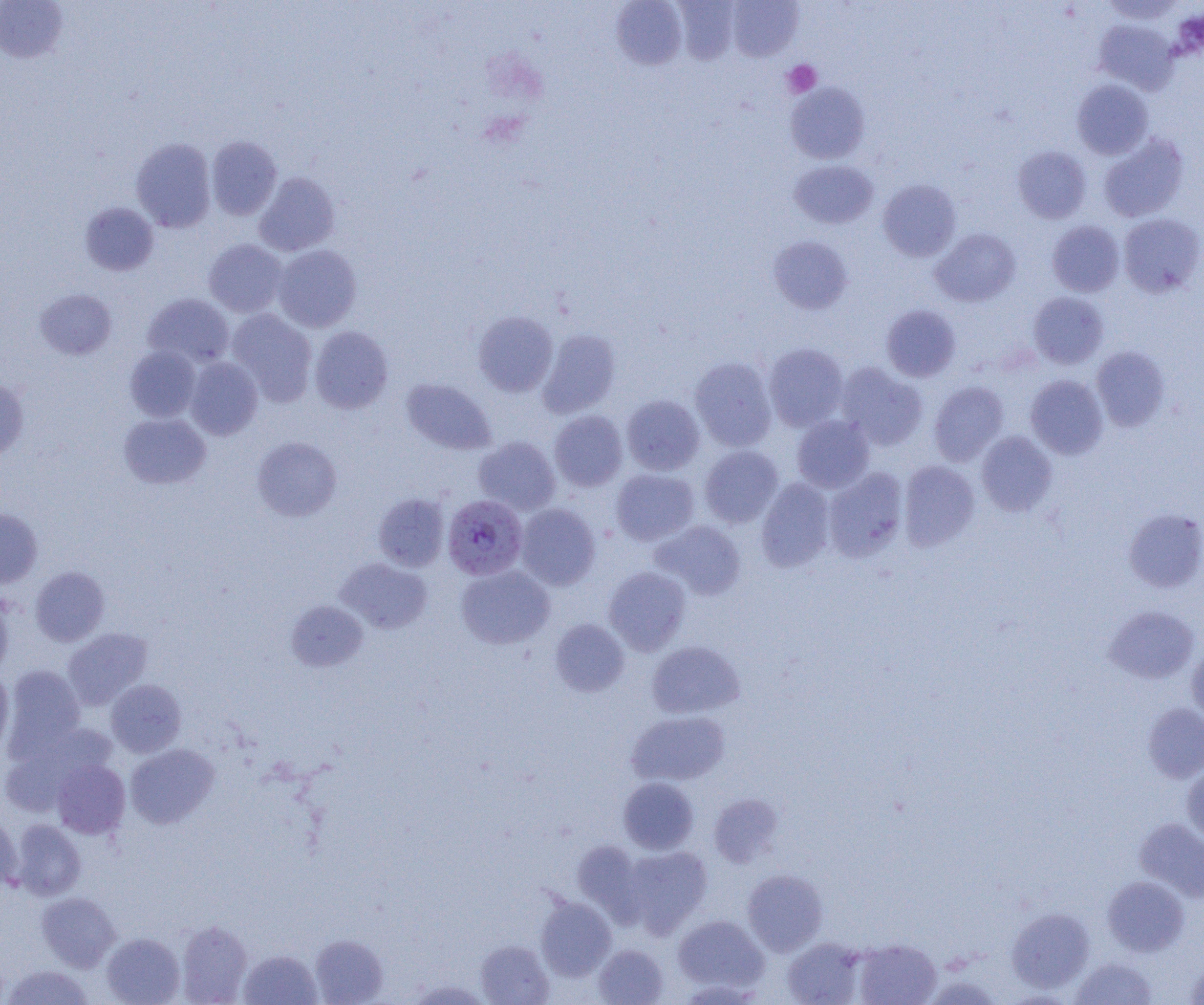
Summary:
  - Coordinate format: approximate bounding boxes as (x1, y1, x2, y2) in pixels
  - Uninfected red blood cell locations: (726, 0, 803, 61), (0, 1, 68, 63), (611, 1, 687, 70), (673, 1, 740, 64), (1093, 19, 1179, 95), (1072, 79, 1153, 159), (785, 82, 871, 164), (1098, 133, 1189, 222), (206, 136, 282, 220), (131, 137, 216, 232), (1013, 146, 1091, 223), (789, 159, 879, 229), (255, 172, 340, 256), (878, 179, 961, 261), (80, 202, 159, 276), (1118, 213, 1204, 297), (1047, 220, 1124, 296), (930, 228, 1021, 307), (769, 235, 853, 314), (203, 239, 288, 317), (273, 245, 361, 332), (35, 288, 117, 359), (1028, 292, 1109, 369), (143, 293, 234, 367), (881, 304, 961, 382), (227, 309, 317, 405), (473, 311, 558, 397), (309, 326, 393, 413), (537, 329, 621, 418), (763, 343, 849, 431), (125, 345, 201, 422), (1092, 346, 1170, 431), (184, 357, 262, 440), (690, 357, 777, 451), (836, 362, 928, 450), (1025, 375, 1108, 459), (0, 376, 30, 458), (401, 378, 496, 455), (929, 381, 1009, 466), (622, 395, 704, 475), (549, 410, 628, 492), (118, 413, 211, 489), (792, 415, 874, 493), (976, 431, 1058, 516), (473, 436, 560, 515), (252, 437, 341, 521), (699, 445, 783, 528), (898, 460, 980, 550), (824, 467, 908, 561), (611, 468, 699, 546), (756, 478, 835, 571), (373, 493, 449, 571), (515, 503, 600, 590), (0, 508, 43, 588), (1124, 508, 1204, 592), (651, 520, 746, 600), (336, 557, 432, 634), (456, 565, 555, 649), (30, 567, 109, 646), (603, 567, 691, 655), (0, 592, 13, 680), (286, 600, 368, 671), (1104, 605, 1199, 684), (550, 619, 629, 696), (62, 628, 152, 710), (646, 641, 745, 719), (1186, 645, 1204, 725), (3, 664, 85, 759), (0, 670, 14, 754), (106, 679, 186, 757), (1142, 703, 1204, 783), (626, 710, 729, 786), (1, 724, 112, 815), (125, 743, 219, 828), (51, 759, 130, 838), (1182, 763, 1204, 845), (619, 777, 699, 854), (709, 794, 784, 867), (0, 811, 21, 893), (1135, 818, 1204, 901), (11, 820, 85, 900), (573, 841, 646, 920), (621, 845, 713, 936), (742, 869, 828, 955), (1102, 876, 1189, 956), (37, 892, 120, 971), (536, 896, 616, 981), (1007, 908, 1094, 993), (673, 915, 769, 994), (177, 920, 252, 1004), (102, 932, 184, 1005), (311, 935, 388, 1004), (782, 937, 866, 1004), (476, 939, 553, 1004), (854, 939, 941, 1005), (593, 944, 669, 1005), (239, 949, 321, 1005), (1071, 956, 1158, 1005), (1185, 959, 1204, 1004), (4, 964, 94, 1005), (406, 979, 492, 1004)
  - Plasmodium falciparum-infected red blood cell locations: (443, 494, 528, 580)
  - Platelet locations: (782, 60, 821, 97)
  - Slide-level diagnosis: Plasmodium falciparum
  - Magnification: 1000x
  - Field of view: one of a larger specimen
  - Image size: 1204×1005 pixels
  - Modality: optical microscopy
  - Preparation: thin blood film